Describe the morphology of the red blood cells.
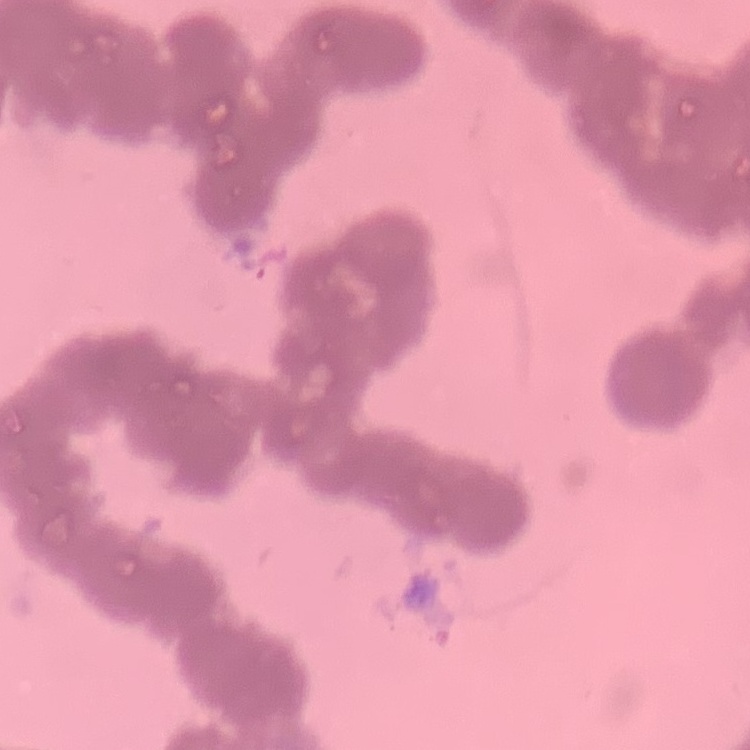
Rouleaux formation.

{
  "image_type": "square crop of a larger photomicrograph",
  "preparation": "thin peripheral smear",
  "stain": "Field's or Giemsa"
}